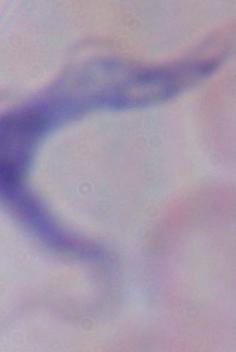

{
  "identification": "trypanosome",
  "modality": "photomicrograph",
  "magnification": "1000x"
}